Locate every uninfected red blood cell.
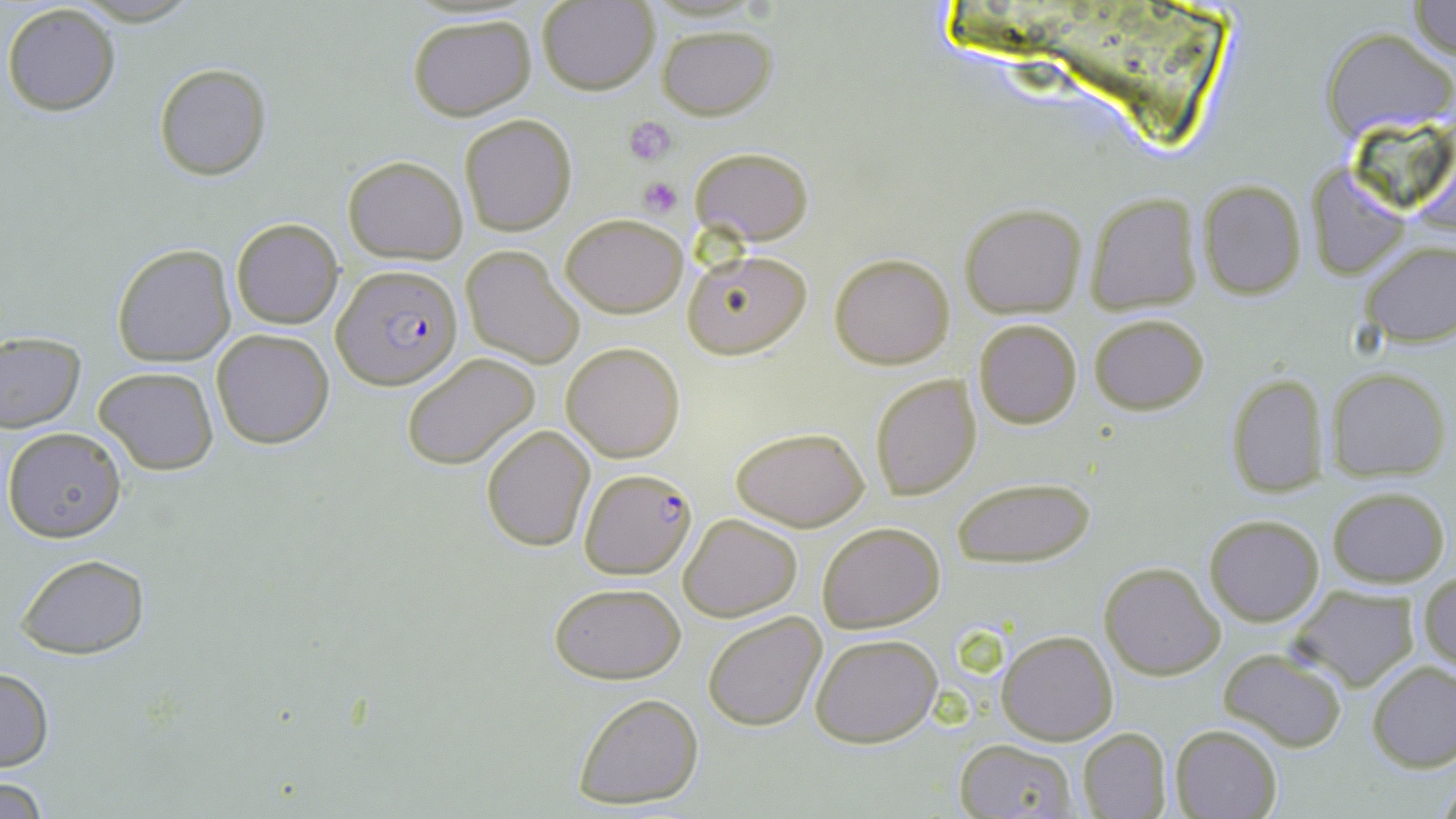

Approximate bounding boxes as [x1, y1, x2, y2] in pixels.
Uninfected red blood cells: [1407, 0, 1456, 62], [538, 1, 659, 94], [2, 3, 121, 117], [406, 13, 536, 120], [658, 25, 775, 120], [1324, 27, 1455, 141], [153, 63, 271, 181], [458, 112, 577, 237], [690, 146, 813, 245], [343, 156, 467, 264], [1307, 164, 1411, 281], [1197, 180, 1306, 299], [1083, 193, 1203, 314], [960, 203, 1087, 317], [560, 212, 689, 318], [230, 217, 343, 330], [1358, 240, 1455, 346], [112, 243, 236, 367], [460, 245, 583, 368], [684, 249, 813, 360], [829, 253, 956, 369], [1089, 313, 1210, 415], [973, 318, 1083, 429], [212, 328, 334, 450], [0, 331, 84, 433], [561, 342, 686, 462], [400, 353, 542, 470], [93, 365, 219, 477], [1327, 366, 1450, 481], [869, 372, 982, 501], [1224, 372, 1330, 497], [481, 424, 596, 552], [730, 425, 870, 531], [3, 427, 126, 543], [952, 474, 1096, 568], [1327, 486, 1449, 586], [1203, 513, 1323, 625], [679, 514, 802, 622], [817, 522, 945, 633], [14, 554, 151, 657], [1100, 561, 1223, 680], [1419, 573, 1456, 675], [550, 582, 685, 682], [1286, 584, 1421, 692], [703, 611, 826, 733], [998, 630, 1116, 745], [811, 633, 942, 748], [1218, 647, 1348, 751], [1368, 660, 1456, 772], [0, 667, 54, 771], [572, 692, 705, 809], [1169, 724, 1282, 819], [1078, 729, 1172, 817], [953, 739, 1082, 818], [2, 777, 52, 817].

Summary:
  - Platelet locations: [624, 118, 677, 167], [637, 175, 683, 218]
  - Plasmodium falciparum-infected red blood cell locations: [335, 264, 463, 391], [577, 468, 695, 578]
  - Slide-level diagnosis: Plasmodium falciparum
  - Field of view: one of a larger specimen
  - Modality: light microscopy
  - Magnification: 1000x
  - Stain: May-Grünwald-Giemsa
  - Preparation: thin blood film
  - Image size: 1456×819 pixels